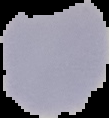

Summary:
  - Image size: 109×118 pixels
  - Result: negative for Plasmodium parasites
  - Image type: cell region segmented out of the field of view; surrounding area masked to black
  - Preparation: thin blood smear